Identify the parasite.
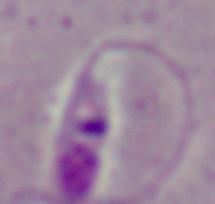
Leishmania.

Micrograph. Captured at 1000x magnification.